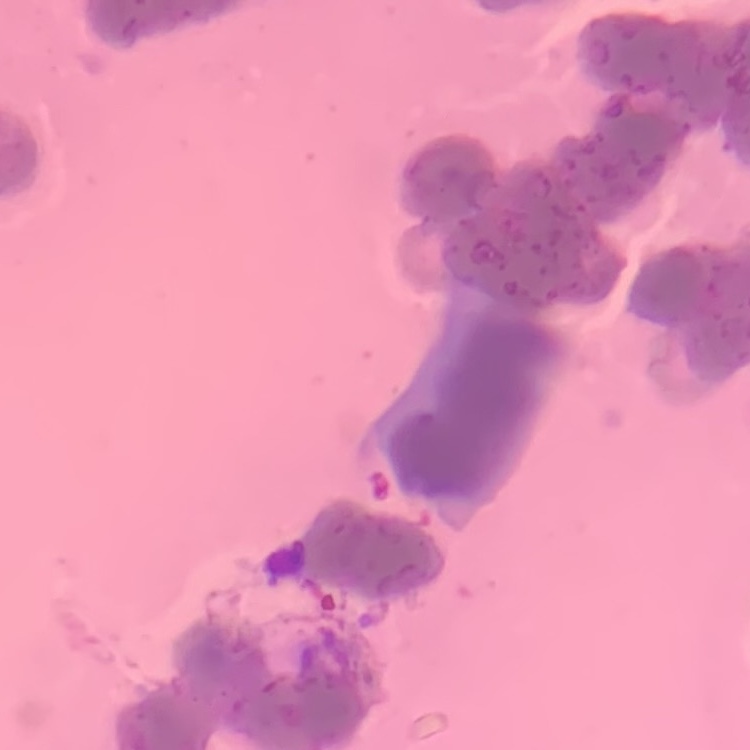
erythrocyte_morphology: rouleaux formation
image_type: one tile cut from a larger photomicrograph
preparation: thin blood film
stain: Field's or Giemsa